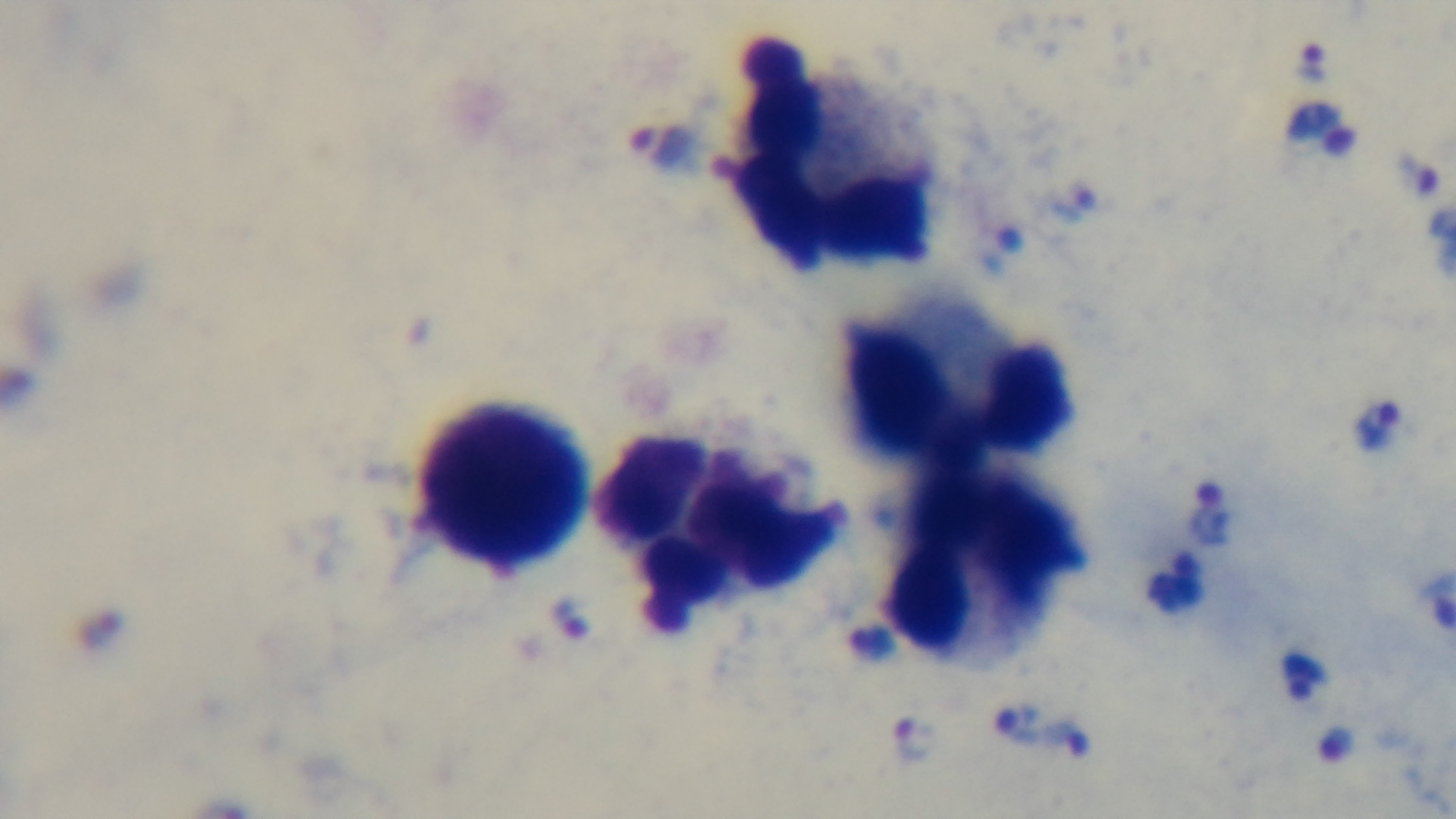
Summary:
  - Objective: 100x oil immersion
  - Malaria status: positive
  - Stain: Giemsa
  - Capture: mounted 4K digital camera
  - Preparation: thick
  - Field of view: one from the slide
  - Modality: light microscopy